Classify this cell by malaria status.
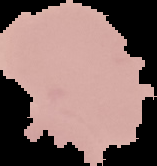

It is uninfected.

Summary:
  - Preparation: thin blood film
  - Image type: cell region segmented out of the field of view; surrounding area masked to black
  - Image size: 157×166 pixels